Comment on the morphology of the red blood cells.
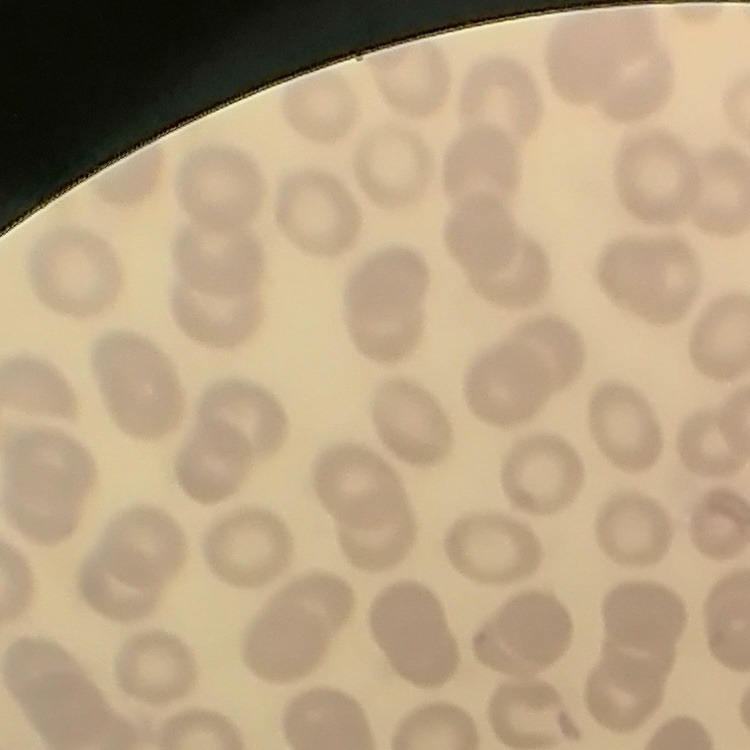
No rouleaux formation.

stain = Field's or Giemsa
preparation = thin peripheral smear
image type = one tile cut from a larger photomicrograph